Locate and identify every blood parasite.
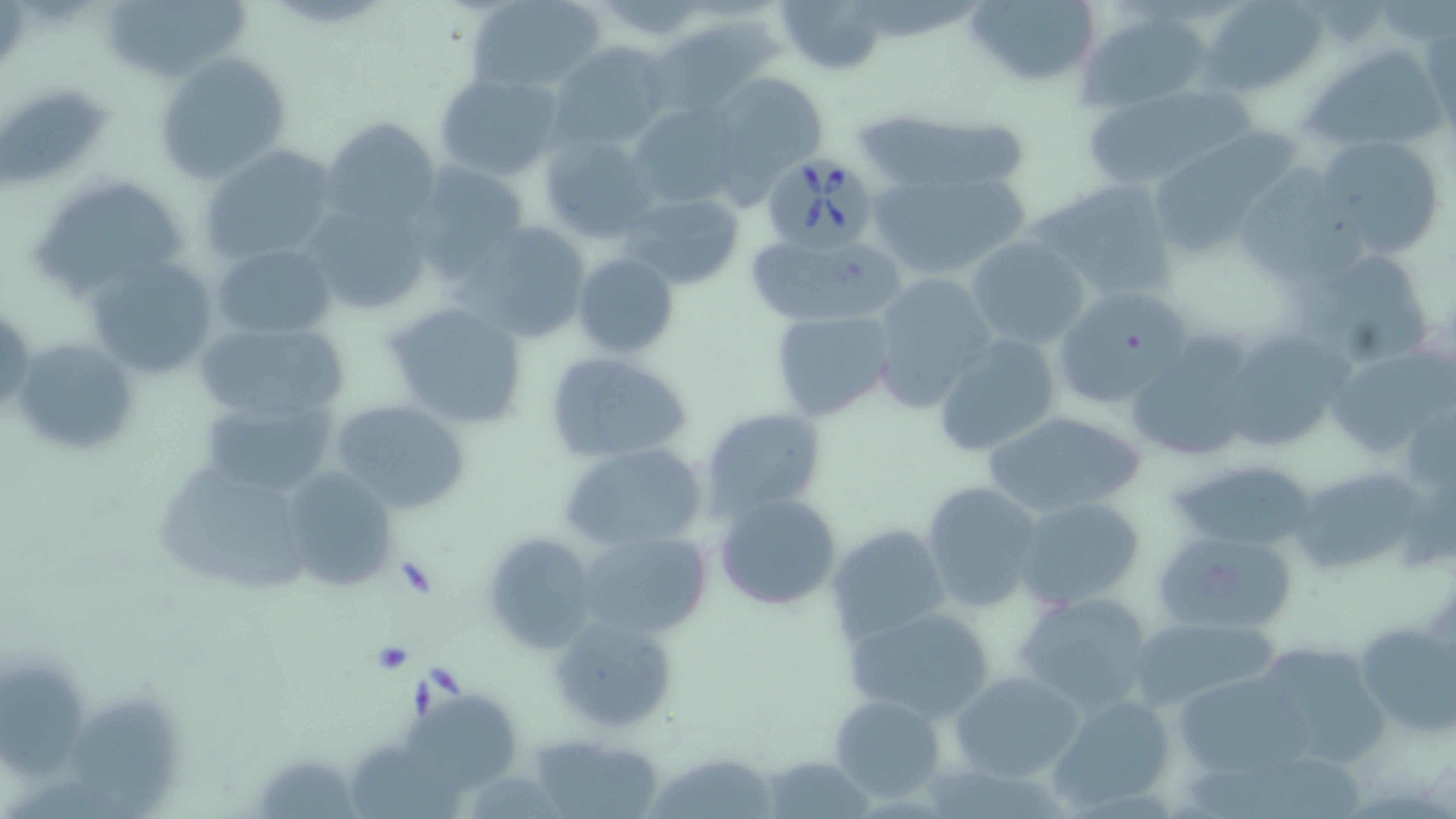
Approximate bounding boxes as (x1, y1, x2, y2) in pixels.
Babesia divergens-infected red blood cells: (754, 156, 882, 247).
No Plasmodium falciparum, Plasmodium ovale, Plasmodium malariae, Plasmodium vivax, or Trypanosoma brucei observed.

Uninfected red blood cell locations: (106, 0, 256, 75), (467, 0, 605, 93), (778, 0, 888, 76), (965, 0, 1103, 90), (1201, 0, 1328, 96), (1079, 8, 1213, 112), (653, 14, 778, 114), (548, 41, 670, 151), (1302, 51, 1449, 142), (153, 53, 292, 185), (433, 71, 564, 180), (703, 72, 827, 191), (1083, 91, 1240, 189), (627, 103, 741, 207), (896, 112, 1033, 195), (323, 115, 441, 228), (1153, 134, 1298, 260), (1315, 135, 1447, 259), (538, 136, 657, 241), (199, 142, 341, 267), (412, 162, 531, 272), (1231, 164, 1363, 281), (867, 165, 1034, 284), (31, 176, 192, 297), (1031, 179, 1179, 301), (618, 190, 748, 294), (299, 199, 435, 317), (463, 219, 593, 344), (744, 232, 901, 329), (966, 236, 1092, 348), (214, 244, 336, 340), (1299, 249, 1441, 370), (572, 251, 679, 359), (86, 254, 221, 378), (869, 273, 997, 414), (1052, 287, 1190, 408), (1, 298, 33, 420), (385, 302, 530, 429), (769, 309, 895, 423), (194, 323, 351, 426), (1225, 330, 1343, 454), (934, 333, 1062, 457), (11, 336, 139, 459), (1124, 342, 1253, 465), (1329, 348, 1456, 457), (544, 351, 694, 463), (200, 395, 340, 503), (331, 399, 473, 514), (701, 407, 828, 517), (979, 408, 1146, 520), (556, 441, 708, 550), (1172, 459, 1322, 551), (153, 460, 314, 596), (1294, 466, 1439, 571), (281, 467, 401, 592), (920, 481, 1045, 615), (714, 491, 845, 612), (1014, 497, 1146, 610), (827, 523, 949, 644), (577, 529, 710, 640), (481, 532, 599, 657), (1149, 533, 1299, 633), (1013, 591, 1155, 717), (849, 608, 996, 723), (547, 614, 677, 734), (1347, 616, 1455, 742), (1127, 618, 1280, 713), (1258, 647, 1394, 770), (0, 666, 90, 788), (1171, 670, 1310, 781), (949, 671, 1086, 782), (829, 692, 946, 804), (68, 694, 182, 815), (1049, 694, 1179, 813), (399, 701, 524, 795), (530, 734, 667, 819), (344, 743, 462, 819), (645, 751, 783, 819), (762, 756, 872, 818). Slide-level diagnosis: Babesia divergens. One field of a larger specimen. May-Grünwald-Giemsa stain. Thin blood film. Captured at 1000x magnification. Image is 1456×819 pixels. Light microscopy.